Point out each Plasmodium parasite and each leukocyte.
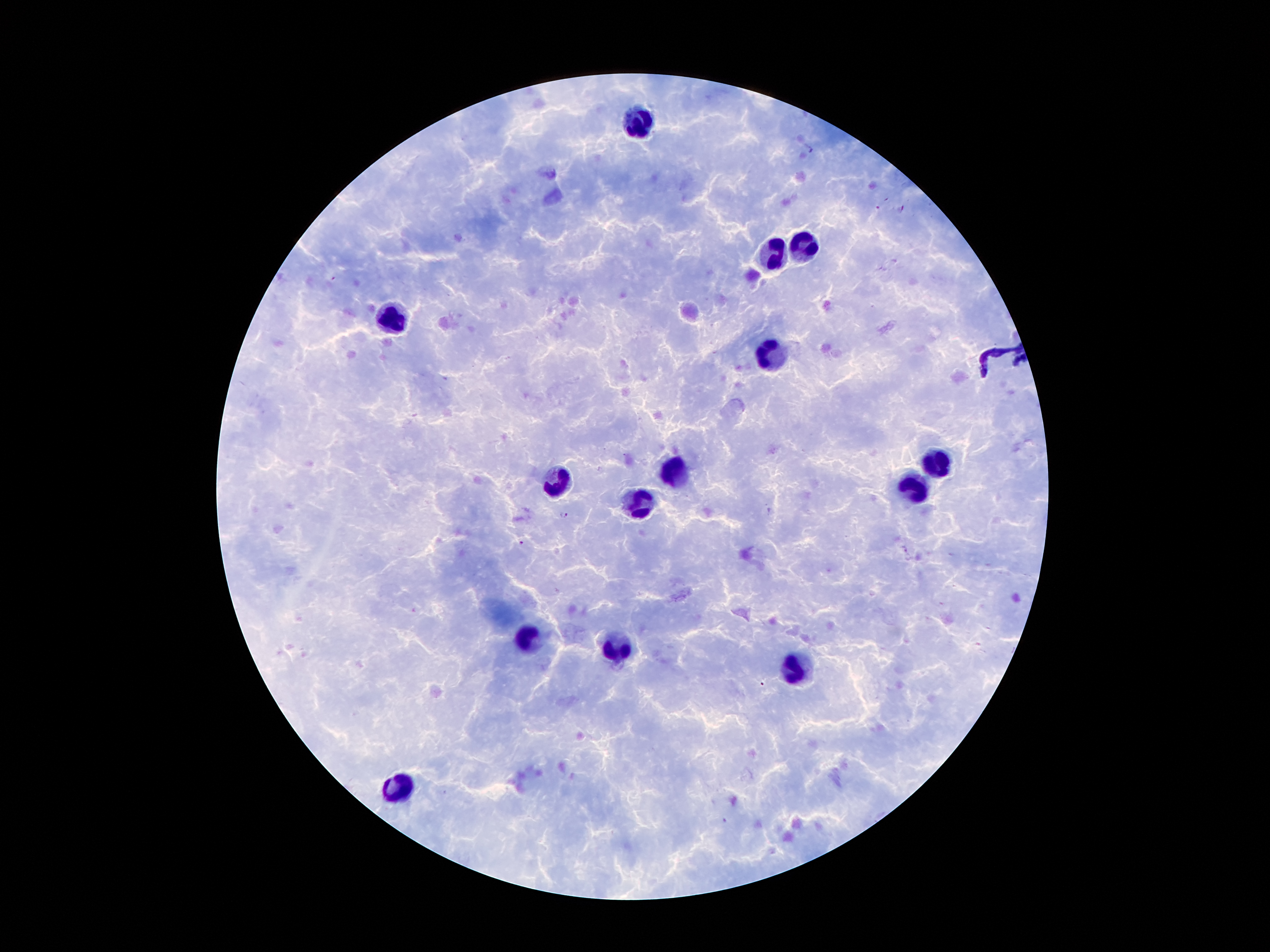

Approximate centers as {x, y} in pixels.
Plasmodium parasites: {810, 147}, {877, 208}, {901, 208}, {563, 514}, {522, 542}.
Leukocytes: {633, 123}, {804, 249}, {773, 259}, {395, 320}, {776, 352}, {938, 462}, {671, 474}, {555, 480}, {914, 488}, {642, 503}, {529, 640}, {619, 646}, {793, 668}, {399, 785}.

Summary:
  - Capture: smartphone through the microscope eyepiece
  - Patient malaria status: infected with Plasmodium falciparum
  - Magnification: 100x
  - Image size: 1270×952 pixels
  - Field of view: one from this slide
  - Preparation: thick peripheral-blood smear
  - Stain: Giemsa